Assess the morphology of the erythrocytes.
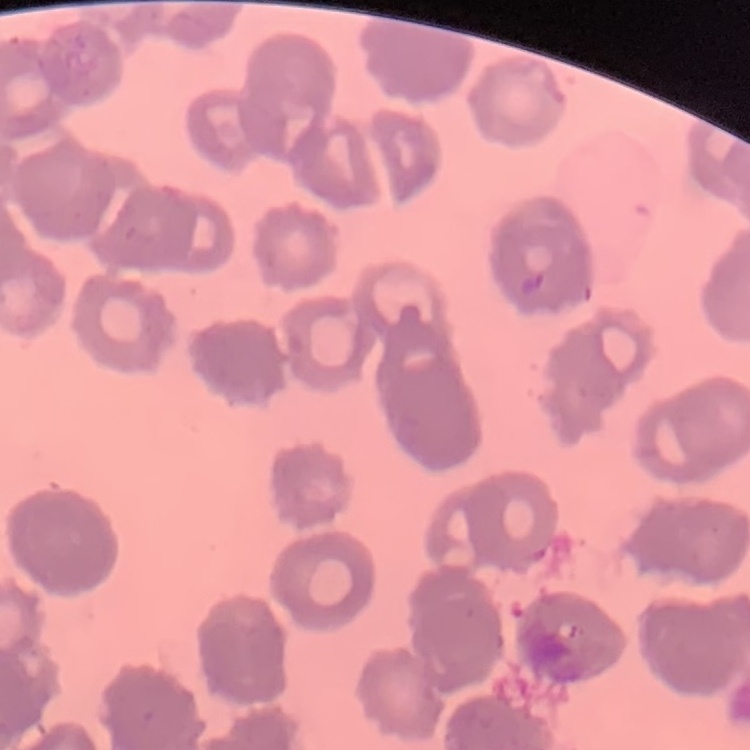

They show rouleaux formation.

Thin blood film. Stained with either Field's or Giemsa. Square crop of a larger photomicrograph.